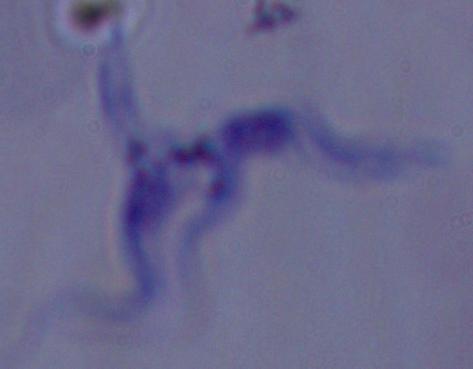
Summary:
  - Modality: micrograph
  - Magnification: 1000x
  - Identification: trypanosome